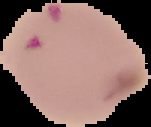 Image is 151×127 pixels. Segmented cell region on a black background. From a thin blood film. Malaria status: parasitized.